Describe the morphology of the red blood cells.
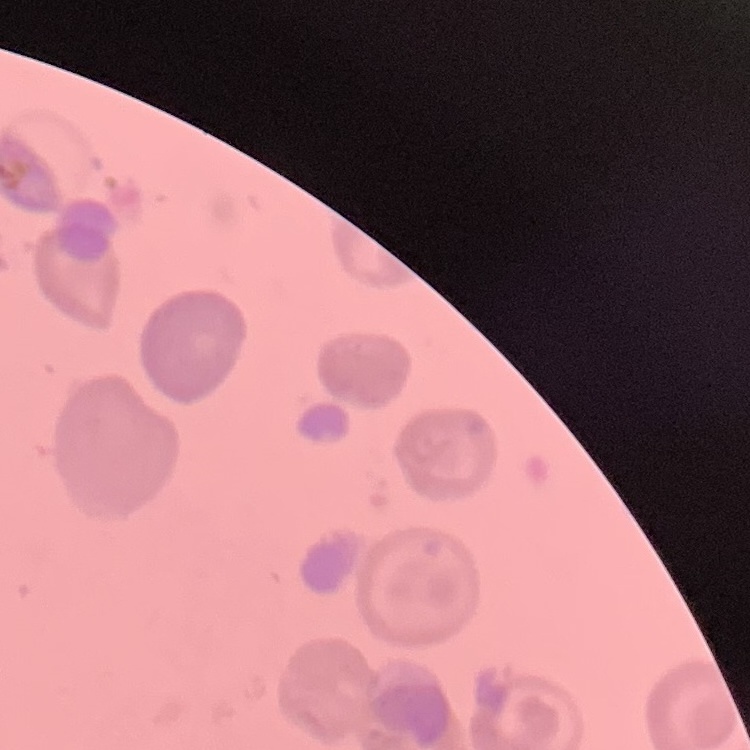

No rouleaux formation.

Thin peripheral smear. Stained with either Field's or Giemsa. Square crop of a larger photomicrograph.